Assess the background quality.
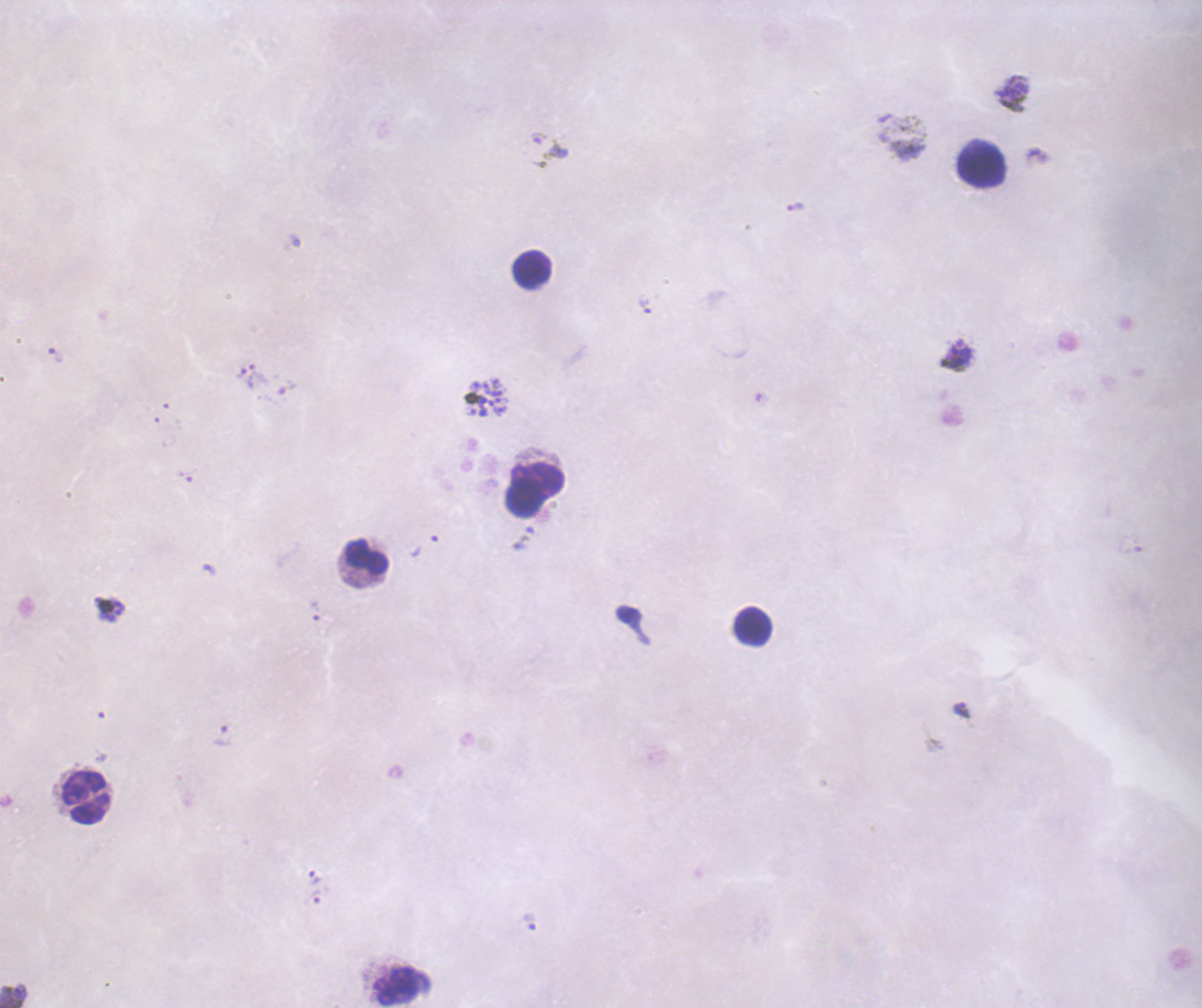

Unsatisfactory.

Approximate centers as (x, y) in pixels.
Summary:
  - Gametocyte locations: (549, 150)
  - Trophozoite locations: (795, 207), (645, 306), (56, 355), (958, 355), (246, 378), (424, 544), (315, 610), (962, 711), (222, 735), (314, 878), (315, 897), (530, 920), (13, 996)
  - Schizont locations: (490, 397)
  - Leukocyte locations: (981, 164), (532, 270), (534, 491), (367, 556), (752, 626), (87, 799), (401, 985)
  - Life-cycle stages observed: trophozoite, schizont, gametocyte
  - Preparation: thick smear of blood
  - Field of view: one from this slide
  - Image size: 1202×1008 pixels
  - Context: previously used in an actual diagnosis
  - Coloration quality: bad
  - Result: positive for malaria parasites
  - Stain: Romanowsky
  - Magnification: 100x